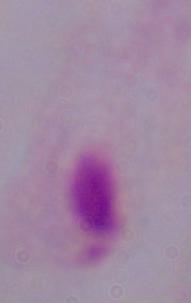

{
  "identification": "trichomonad",
  "modality": "photomicrograph",
  "magnification": "1000x"
}